Report the malaria status of this cell.
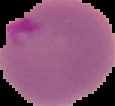
Parasitized.

image_size: 115×106 pixels
preparation: thin blood smear
image_type: segmented cell region with the area outside set to black